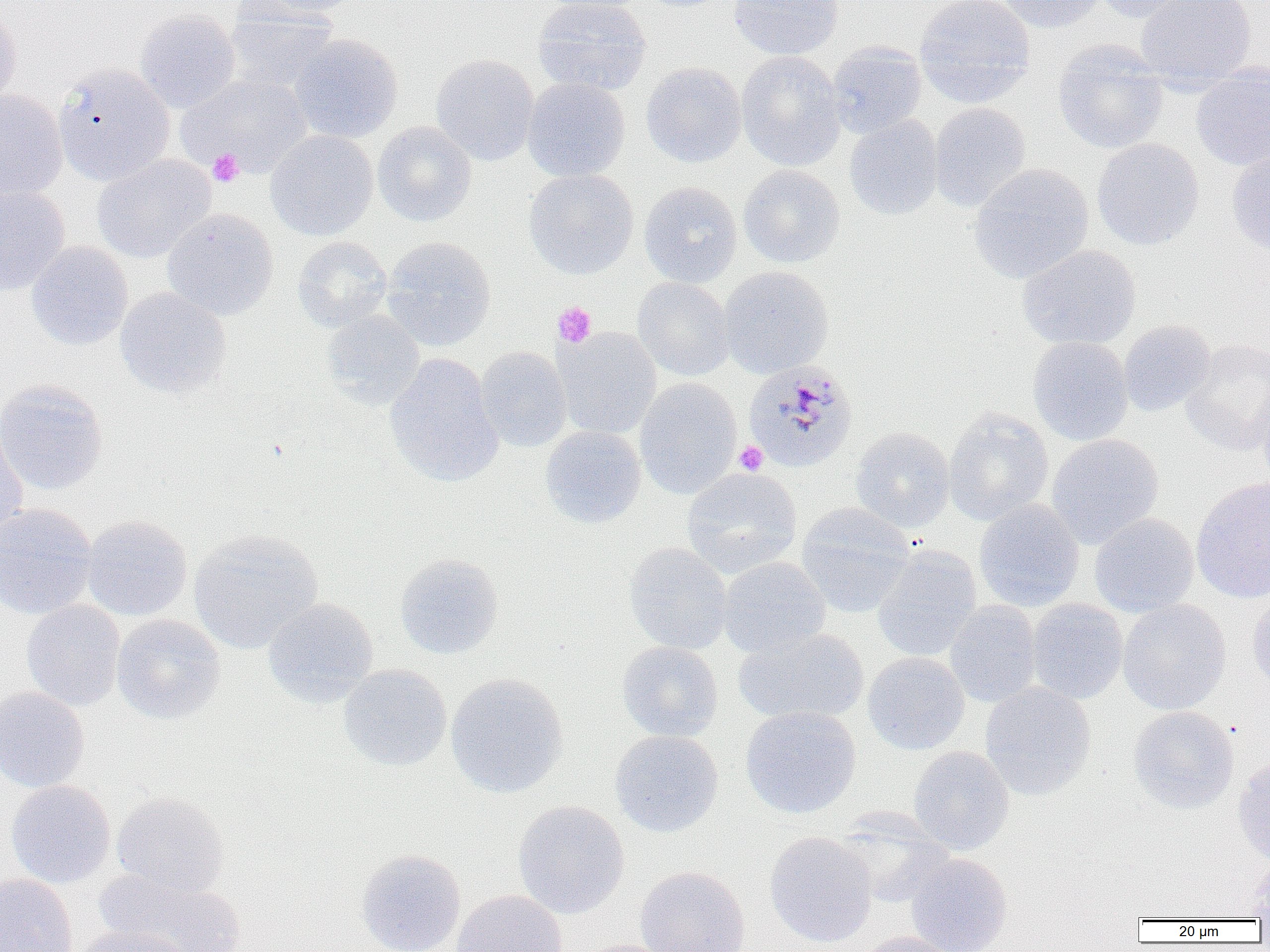
Approximate bounding boxes as named x1/y1/x2/y2 corners in pixels. Uninfected red blood cell locations: (x1=248, y1=0, x2=364, y2=19), (x1=532, y1=0, x2=652, y2=96), (x1=538, y1=0, x2=656, y2=13), (x1=636, y1=0, x2=739, y2=12), (x1=728, y1=0, x2=844, y2=60), (x1=914, y1=0, x2=1035, y2=108), (x1=995, y1=0, x2=1108, y2=33), (x1=1087, y1=0, x2=1206, y2=23), (x1=1135, y1=0, x2=1257, y2=89), (x1=0, y1=4, x2=21, y2=110), (x1=222, y1=7, x2=339, y2=95), (x1=134, y1=9, x2=241, y2=112), (x1=287, y1=33, x2=404, y2=144), (x1=1052, y1=39, x2=1168, y2=154), (x1=826, y1=41, x2=927, y2=139), (x1=736, y1=50, x2=846, y2=171), (x1=431, y1=53, x2=538, y2=166), (x1=641, y1=62, x2=746, y2=167), (x1=53, y1=63, x2=174, y2=185), (x1=1191, y1=63, x2=1270, y2=171), (x1=177, y1=73, x2=311, y2=179), (x1=522, y1=77, x2=631, y2=182), (x1=0, y1=90, x2=68, y2=202), (x1=929, y1=102, x2=1031, y2=212), (x1=844, y1=115, x2=944, y2=220), (x1=372, y1=121, x2=477, y2=227), (x1=265, y1=129, x2=378, y2=241), (x1=1092, y1=138, x2=1204, y2=251), (x1=1226, y1=149, x2=1270, y2=258), (x1=91, y1=154, x2=217, y2=264), (x1=968, y1=163, x2=1094, y2=283), (x1=739, y1=164, x2=845, y2=268), (x1=524, y1=168, x2=639, y2=279), (x1=639, y1=181, x2=742, y2=287), (x1=0, y1=183, x2=70, y2=297), (x1=161, y1=208, x2=279, y2=321), (x1=292, y1=236, x2=392, y2=332), (x1=382, y1=236, x2=496, y2=351), (x1=26, y1=242, x2=133, y2=350), (x1=1017, y1=244, x2=1141, y2=350), (x1=718, y1=266, x2=833, y2=378), (x1=632, y1=277, x2=735, y2=381), (x1=114, y1=287, x2=232, y2=399), (x1=320, y1=310, x2=425, y2=410), (x1=1118, y1=320, x2=1216, y2=417), (x1=554, y1=327, x2=662, y2=440), (x1=1028, y1=336, x2=1134, y2=446), (x1=1180, y1=338, x2=1270, y2=455), (x1=474, y1=347, x2=573, y2=452), (x1=384, y1=354, x2=504, y2=488), (x1=635, y1=378, x2=742, y2=498), (x1=0, y1=380, x2=108, y2=496), (x1=1256, y1=385, x2=1270, y2=489), (x1=943, y1=406, x2=1054, y2=526), (x1=0, y1=419, x2=28, y2=544), (x1=540, y1=425, x2=646, y2=528), (x1=850, y1=426, x2=955, y2=532), (x1=1046, y1=433, x2=1164, y2=548), (x1=681, y1=466, x2=803, y2=578), (x1=1191, y1=477, x2=1270, y2=603), (x1=974, y1=499, x2=1084, y2=612), (x1=0, y1=502, x2=98, y2=620), (x1=795, y1=502, x2=916, y2=618), (x1=1089, y1=513, x2=1199, y2=617), (x1=81, y1=514, x2=192, y2=621), (x1=1101, y1=514, x2=1208, y2=714), (x1=189, y1=528, x2=323, y2=654), (x1=623, y1=542, x2=733, y2=655), (x1=872, y1=545, x2=982, y2=662), (x1=394, y1=553, x2=504, y2=659), (x1=717, y1=556, x2=831, y2=658), (x1=1246, y1=591, x2=1270, y2=696), (x1=262, y1=597, x2=378, y2=707), (x1=21, y1=599, x2=126, y2=711), (x1=1026, y1=599, x2=1128, y2=704), (x1=1118, y1=599, x2=1231, y2=715), (x1=944, y1=600, x2=1042, y2=707), (x1=111, y1=614, x2=225, y2=725), (x1=733, y1=627, x2=869, y2=726), (x1=616, y1=641, x2=724, y2=742), (x1=863, y1=652, x2=970, y2=755), (x1=338, y1=665, x2=452, y2=772), (x1=445, y1=673, x2=569, y2=798), (x1=980, y1=682, x2=1096, y2=799), (x1=0, y1=686, x2=89, y2=793), (x1=1127, y1=705, x2=1239, y2=814), (x1=740, y1=706, x2=861, y2=818), (x1=609, y1=730, x2=723, y2=838), (x1=908, y1=746, x2=1014, y2=855), (x1=1233, y1=756, x2=1270, y2=865), (x1=5, y1=779, x2=116, y2=889), (x1=111, y1=791, x2=230, y2=897), (x1=512, y1=800, x2=630, y2=919), (x1=836, y1=812, x2=956, y2=909), (x1=764, y1=831, x2=878, y2=948), (x1=356, y1=849, x2=466, y2=952), (x1=905, y1=853, x2=1012, y2=952), (x1=1243, y1=859, x2=1270, y2=919), (x1=635, y1=865, x2=751, y2=952), (x1=96, y1=870, x2=245, y2=952), (x1=0, y1=873, x2=78, y2=952), (x1=451, y1=890, x2=569, y2=952), (x1=67, y1=925, x2=192, y2=952), (x1=851, y1=931, x2=966, y2=952), (x1=571, y1=939, x2=680, y2=952). Plasmodium malariae-infected red blood cell locations: (x1=742, y1=360, x2=858, y2=473). Platelet locations: (x1=207, y1=149, x2=244, y2=187), (x1=552, y1=302, x2=596, y2=348), (x1=734, y1=441, x2=768, y2=475). Slide-level diagnosis: Plasmodium malariae. 1000x magnification. One field of a larger specimen. Thin blood film. Light microscopy. Image is 1270×952 pixels.